Locate every Plasmodium falciparum-infected red blood cell.
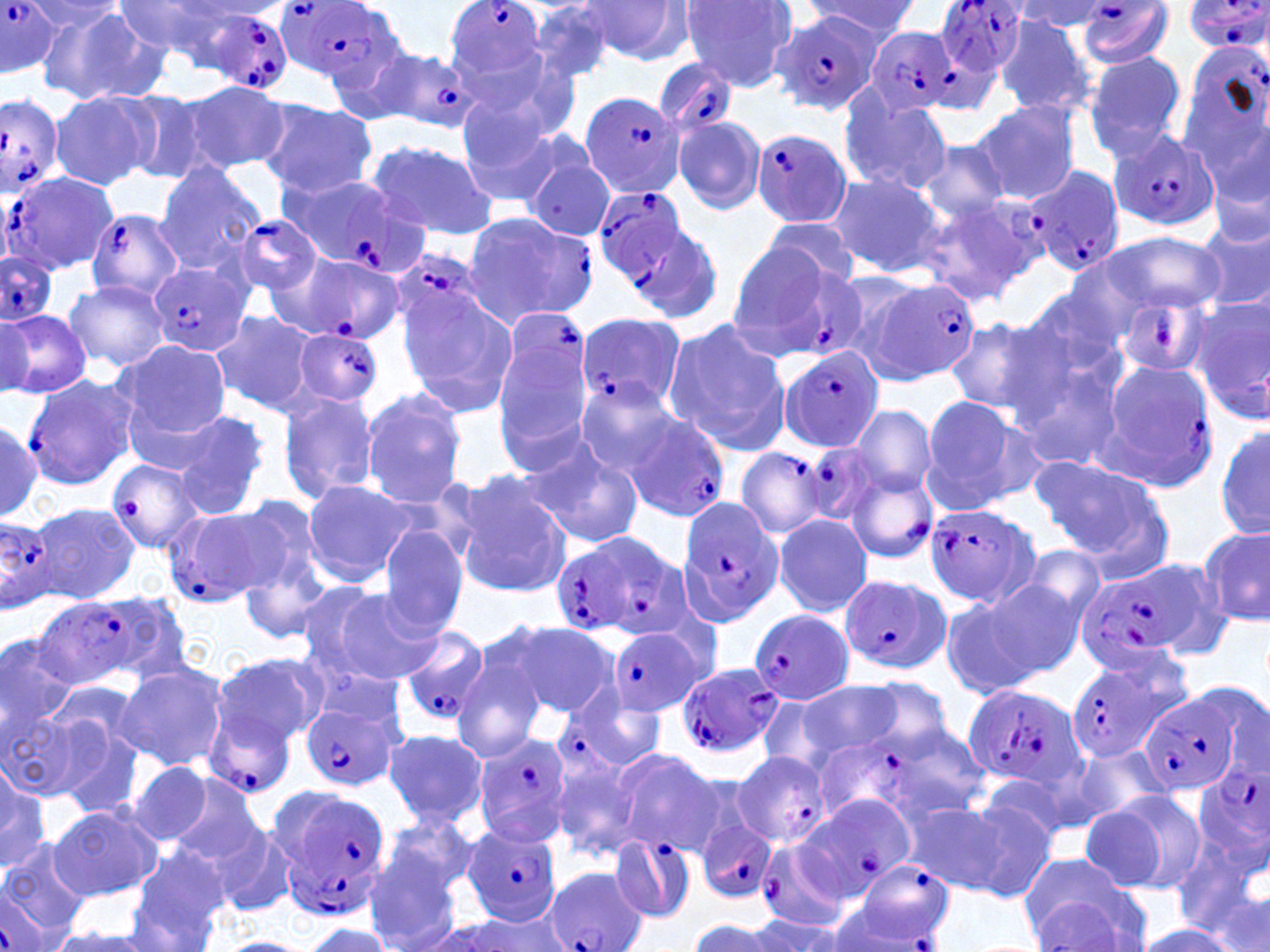
Approximate bounding boxes as (x1,y1)-(x2,y2) corner pairs in pixels.
Plasmodium falciparum-infected red blood cells: (277,0)-(400,84), (442,0)-(547,84), (929,0)-(1032,77), (1074,0)-(1175,69), (1181,0)-(1270,55), (0,2)-(61,77), (208,11)-(294,93), (769,12)-(878,115), (861,26)-(960,119), (371,49)-(482,133), (653,59)-(739,137), (577,89)-(686,200), (0,91)-(63,202), (750,128)-(852,228), (1109,129)-(1223,232), (1024,169)-(1124,275), (1,173)-(120,275), (277,173)-(422,272), (593,185)-(692,284), (914,193)-(1044,307), (86,208)-(185,302), (461,210)-(597,330), (233,215)-(322,296), (622,216)-(725,329), (0,251)-(57,326), (394,252)-(479,330), (277,253)-(400,341), (151,262)-(251,357), (777,263)-(869,357), (869,278)-(982,381), (509,310)-(583,389), (576,314)-(686,415), (292,326)-(384,406), (778,345)-(885,454), (1097,360)-(1217,492), (23,373)-(136,491), (623,413)-(727,521), (800,440)-(887,529), (735,447)-(827,540), (104,459)-(207,554), (844,468)-(938,565), (676,496)-(785,626), (163,503)-(287,607), (922,504)-(1041,607), (0,517)-(56,610), (550,531)-(686,640), (1075,562)-(1207,671), (841,576)-(950,675), (32,597)-(141,689), (749,609)-(856,705), (608,626)-(704,718), (398,628)-(491,724), (674,661)-(784,760), (1068,661)-(1173,763), (200,684)-(307,800), (559,685)-(668,776), (961,686)-(1084,790), (1139,694)-(1236,794), (301,698)-(403,794), (811,730)-(936,824), (471,732)-(573,846), (730,750)-(832,849), (1193,763)-(1269,866), (272,785)-(391,920), (801,791)-(915,898), (696,819)-(777,904), (465,823)-(563,929), (610,835)-(696,923), (754,837)-(854,931), (837,865)-(959,951), (545,868)-(649,952), (1,892)-(52,951).

Uninfected red blood cell locations: (116,0)-(250,69), (578,0)-(694,65), (678,0)-(797,91), (22,1)-(127,43), (804,1)-(918,40), (1011,1)-(1110,35), (528,3)-(619,86), (41,6)-(168,106), (1083,51)-(1187,160), (463,54)-(579,152), (182,82)-(289,174), (119,88)-(220,184), (48,90)-(159,191), (838,91)-(953,197), (256,98)-(378,199), (456,100)-(569,205), (969,100)-(1081,205), (673,115)-(767,214), (520,139)-(614,241), (366,141)-(497,239), (914,141)-(1013,225), (1208,153)-(1270,255), (154,161)-(265,271), (825,172)-(944,277), (761,216)-(861,292), (1197,219)-(1270,317), (1101,230)-(1225,316), (723,241)-(828,332), (818,269)-(934,372), (63,278)-(169,373), (1011,289)-(1130,399), (1114,292)-(1212,379), (393,296)-(519,426), (1191,299)-(1270,424), (210,307)-(324,420), (0,308)-(90,402), (0,310)-(33,399), (943,315)-(1063,419), (663,316)-(792,458), (1003,338)-(1128,469), (112,339)-(231,452), (491,345)-(596,462), (575,380)-(684,476), (359,384)-(469,508), (277,389)-(380,504), (917,394)-(1045,513), (850,404)-(939,499), (173,411)-(270,521), (0,420)-(42,520), (1216,422)-(1269,540), (522,439)-(645,549), (1029,455)-(1169,569), (450,473)-(574,597), (300,479)-(418,587), (228,495)-(328,604), (26,500)-(140,607), (772,514)-(872,617), (377,525)-(470,639), (1198,526)-(1269,629), (236,536)-(332,642), (1016,544)-(1110,633), (977,577)-(1088,679), (329,590)-(445,685), (938,592)-(1045,699), (498,620)-(615,717), (0,631)-(79,738), (450,652)-(548,764), (212,653)-(327,751), (115,661)-(230,772), (860,675)-(956,760), (791,680)-(903,765), (1208,680)-(1270,784), (23,689)-(141,808), (3,707)-(92,802), (877,723)-(992,822), (383,728)-(486,829), (1070,743)-(1173,826), (611,749)-(727,857), (549,752)-(644,861), (126,758)-(214,848), (0,760)-(51,876), (975,769)-(1080,854), (162,775)-(267,875), (1090,789)-(1209,895), (953,798)-(1061,901), (902,802)-(1010,893), (47,805)-(162,900), (380,814)-(477,897), (210,824)-(301,919), (1173,826)-(1270,950), (364,838)-(466,952), (0,841)-(92,942), (126,851)-(229,951), (1027,894)-(1135,950), (444,911)-(575,951), (748,914)-(855,952), (689,919)-(776,951), (299,923)-(397,952), (1131,923)-(1242,951), (42,928)-(165,951), (214,937)-(320,952). Slide-level diagnosis: Plasmodium falciparum. Captured at 1000x magnification. Single field of view. May-Grünwald-Giemsa stain. Thin blood film. Image is 1270×952 pixels. Optical microscopy.